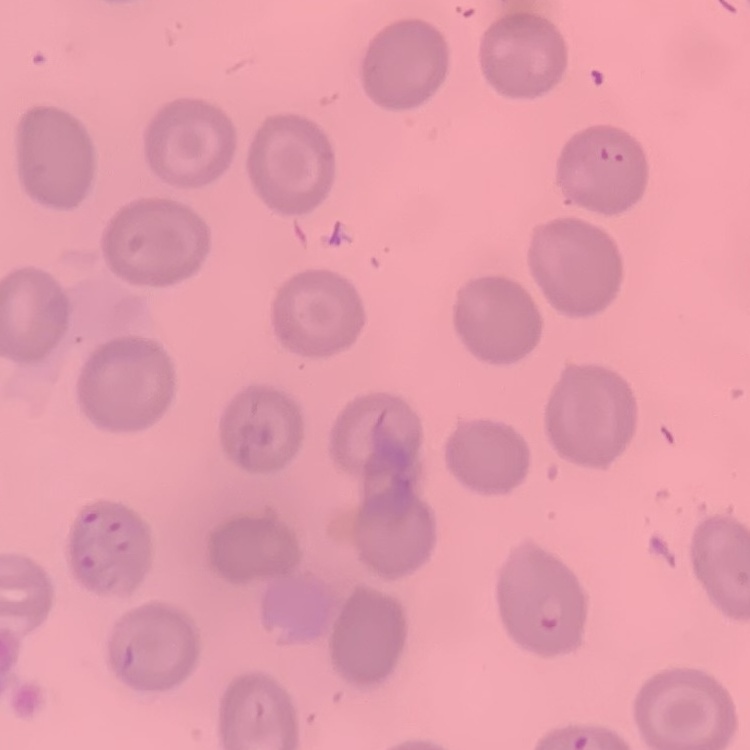

Summary:
  - Erythrocyte morphology: no rouleaux formation
  - Preparation: thin peripheral smear
  - Image type: one tile cut from a larger photomicrograph
  - Stain: Field's or Giemsa